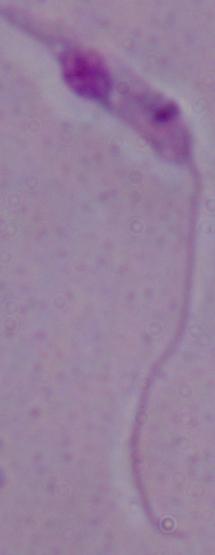
Summary:
  - Magnification: 1000x
  - Identification: Leishmania
  - Modality: micrograph